Give the extent of all uninfected red blood cells.
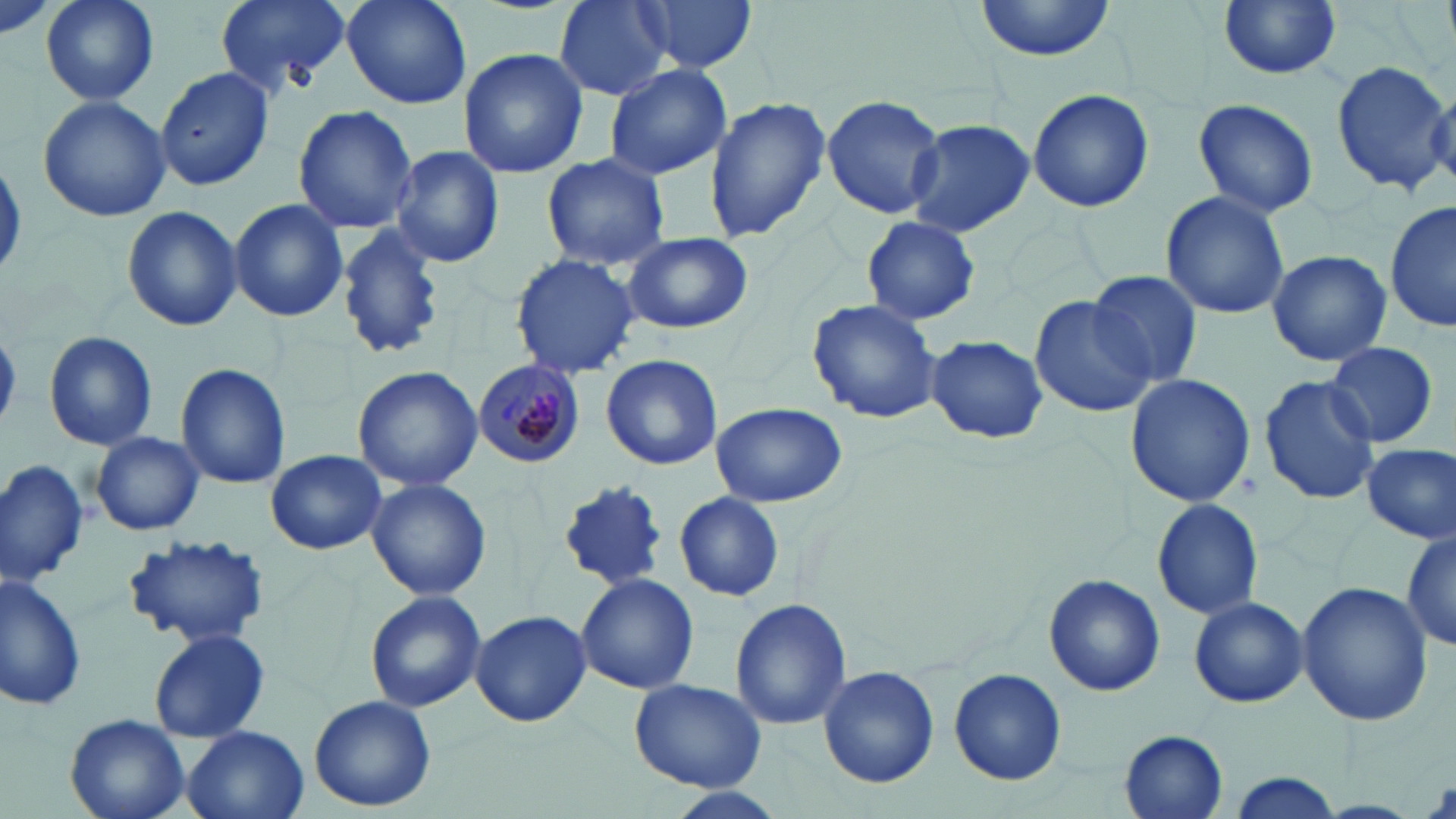

Approximate bounding boxes as named x1/y1/x2/y2 corners in pixels.
Uninfected red blood cells: (x1=42, y1=0, x2=158, y2=106), (x1=215, y1=0, x2=352, y2=93), (x1=338, y1=0, x2=476, y2=111), (x1=554, y1=0, x2=672, y2=100), (x1=634, y1=0, x2=758, y2=74), (x1=972, y1=0, x2=1120, y2=62), (x1=1217, y1=0, x2=1342, y2=80), (x1=459, y1=47, x2=589, y2=177), (x1=1332, y1=57, x2=1456, y2=196), (x1=604, y1=63, x2=732, y2=180), (x1=155, y1=65, x2=274, y2=190), (x1=1026, y1=89, x2=1155, y2=213), (x1=820, y1=93, x2=946, y2=219), (x1=703, y1=95, x2=831, y2=241), (x1=38, y1=96, x2=170, y2=222), (x1=1192, y1=98, x2=1318, y2=217), (x1=293, y1=104, x2=418, y2=233), (x1=905, y1=119, x2=1034, y2=239), (x1=389, y1=145, x2=504, y2=269), (x1=539, y1=153, x2=670, y2=271), (x1=1159, y1=190, x2=1291, y2=320), (x1=227, y1=198, x2=348, y2=322), (x1=1386, y1=198, x2=1455, y2=334), (x1=121, y1=207, x2=242, y2=331), (x1=860, y1=216, x2=982, y2=326), (x1=334, y1=224, x2=446, y2=361), (x1=621, y1=230, x2=754, y2=334), (x1=1265, y1=249, x2=1392, y2=367), (x1=510, y1=253, x2=640, y2=379), (x1=1086, y1=269, x2=1203, y2=389), (x1=1030, y1=295, x2=1157, y2=419), (x1=807, y1=299, x2=944, y2=425), (x1=44, y1=331, x2=156, y2=450), (x1=926, y1=334, x2=1047, y2=444), (x1=1324, y1=343, x2=1440, y2=450), (x1=599, y1=353, x2=724, y2=470), (x1=175, y1=363, x2=291, y2=489), (x1=352, y1=365, x2=482, y2=494), (x1=1124, y1=373, x2=1256, y2=507), (x1=1259, y1=373, x2=1381, y2=504), (x1=710, y1=402, x2=845, y2=508), (x1=91, y1=431, x2=204, y2=534), (x1=1361, y1=444, x2=1455, y2=544), (x1=267, y1=449, x2=385, y2=555), (x1=0, y1=459, x2=88, y2=586), (x1=366, y1=478, x2=490, y2=602), (x1=557, y1=478, x2=670, y2=593), (x1=675, y1=490, x2=784, y2=603), (x1=1152, y1=499, x2=1263, y2=621), (x1=1402, y1=528, x2=1456, y2=650), (x1=123, y1=533, x2=271, y2=646), (x1=1, y1=571, x2=89, y2=711), (x1=1043, y1=572, x2=1164, y2=696), (x1=574, y1=573, x2=700, y2=693), (x1=1296, y1=581, x2=1433, y2=727), (x1=365, y1=590, x2=486, y2=712), (x1=1189, y1=597, x2=1308, y2=708), (x1=731, y1=598, x2=851, y2=729), (x1=471, y1=609, x2=591, y2=727), (x1=150, y1=628, x2=269, y2=742), (x1=819, y1=664, x2=939, y2=788), (x1=950, y1=668, x2=1067, y2=785), (x1=628, y1=676, x2=768, y2=792), (x1=308, y1=694, x2=439, y2=812), (x1=66, y1=714, x2=190, y2=819), (x1=182, y1=726, x2=309, y2=819), (x1=1119, y1=730, x2=1228, y2=818), (x1=1227, y1=772, x2=1343, y2=819), (x1=658, y1=785, x2=789, y2=819).

slide_level_diagnosis: Plasmodium malariae
preparation: thin blood smear
field_of_view: one of a larger specimen
stain: May-Grünwald-Giemsa
modality: optical microscopy
plasmodium_malariae_infected_red_blood_cell_locations: 'approximate bounding boxes as named x1/y1/x2/y2 corners in pixels: (x1=473, y1=359, x2=585, y2=467)'
magnification: 1000x
image_size: 1456×819 pixels